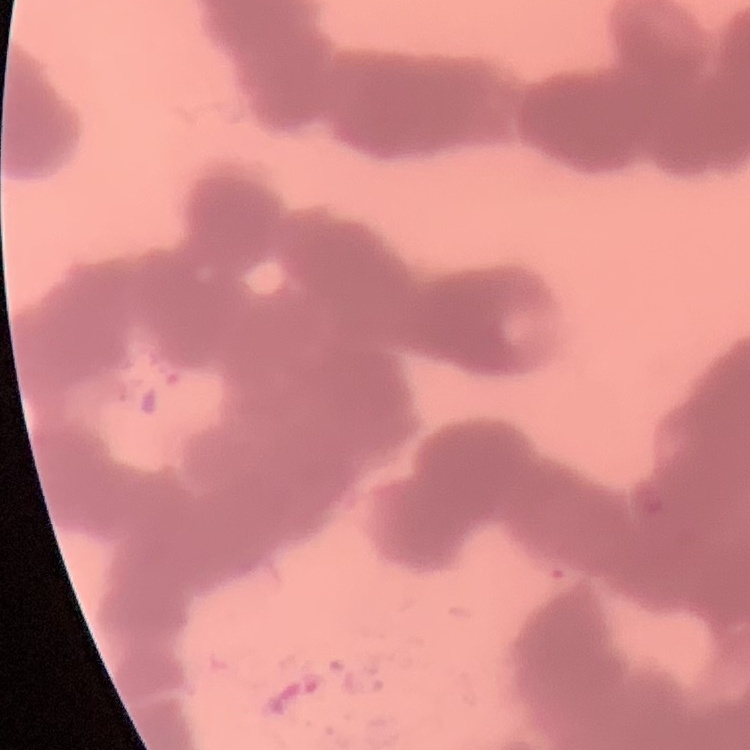 The erythrocytes exhibit rouleaux formation. Field's or Giemsa stain. One tile cut from a larger photomicrograph. Thin blood film.